Identify the parasite.
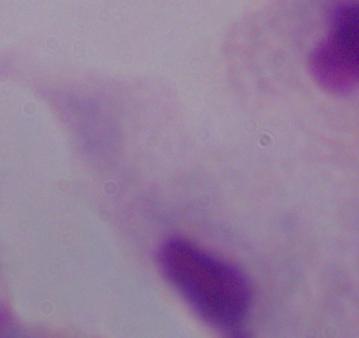
A trichomonad.

Summary:
  - Magnification: 1000x
  - Modality: micrograph